Assess this cell for malaria.
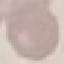
Uninfected.

Thin smear of blood. Photographed with a smartphone camera at the microscope eyepiece. Giemsa-stained preparation. Cell patch, automatically extracted from a larger field of view and resized to 64 × 64 pixels.